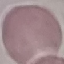
Summary:
  - Result: no malaria parasites seen
  - Image type: cell patch, automatically extracted from a larger field of view and resized to 64 × 64 pixels
  - Preparation: thin smear
  - Stain: Giemsa
  - Capture: smartphone camera at the microscope eyepiece